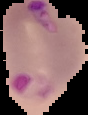
Summary:
  - Image size: 88×115 pixels
  - Preparation: thin blood smear
  - Malaria status: parasitized
  - Image type: segmented cell region with the area outside set to black